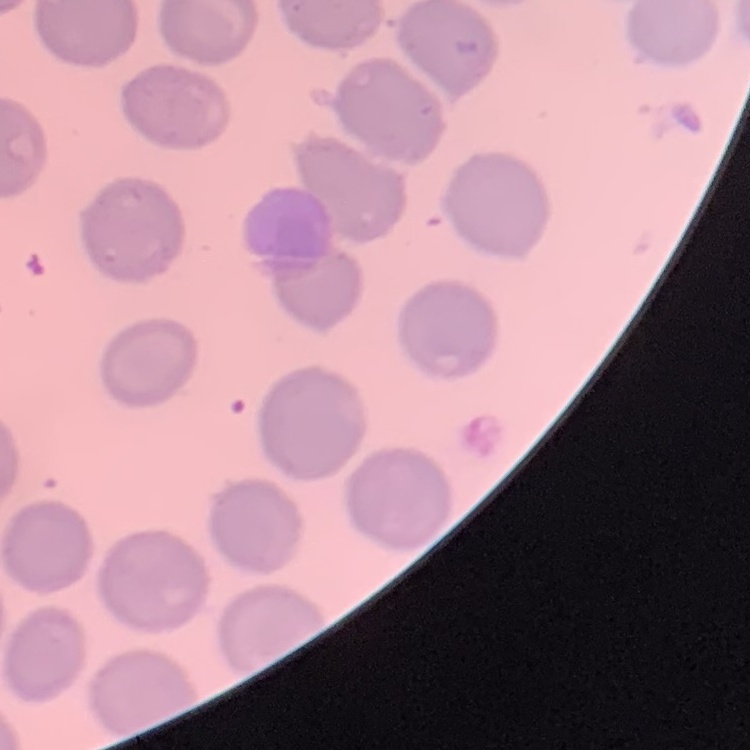

The red blood cells exhibit no rouleaux formation. One tile cut from a larger photomicrograph. Thin peripheral smear. Field's or Giemsa stain.